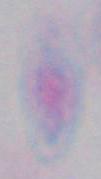

Summary:
  - Identification: Toxoplasma gondii
  - Modality: photomicrograph
  - Magnification: 1000x